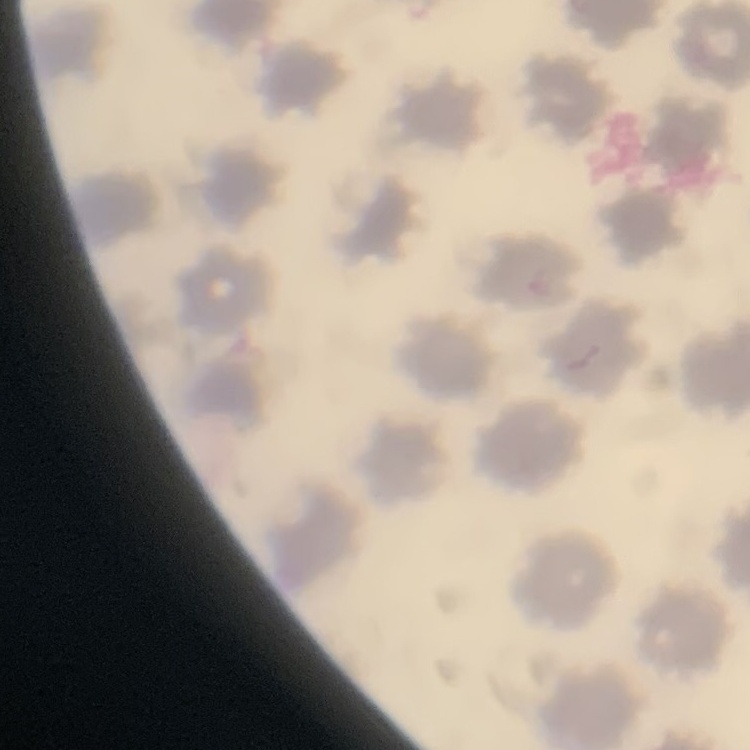
The erythrocytes show no rouleaux formation. Field's or Giemsa stain. Square crop of a larger photomicrograph. Thin blood smear.